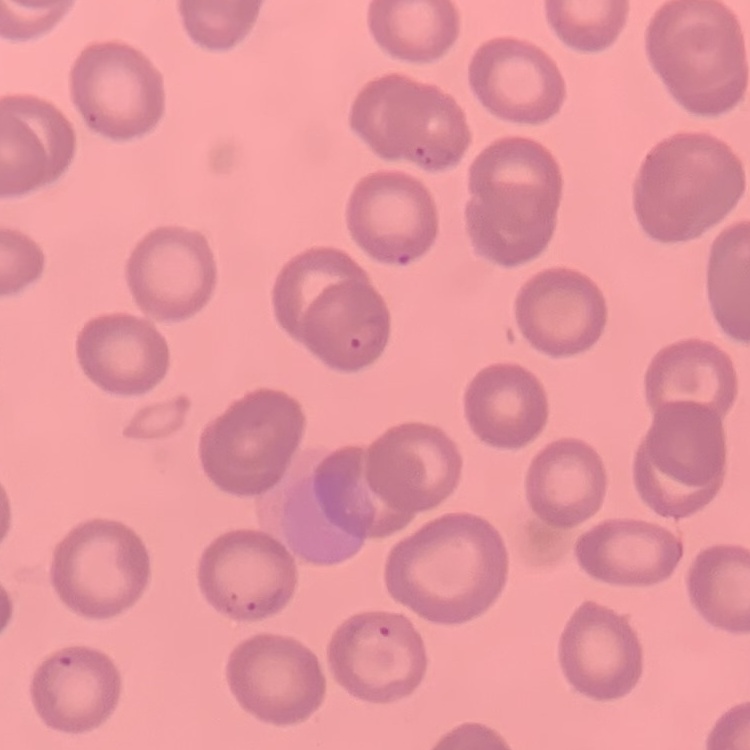
erythrocyte morphology = no rouleaux formation
preparation = thin blood smear
image type = square crop of a larger photomicrograph
stain = Field's or Giemsa